Classify this cell by malaria status.
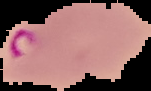

Parasitized.

From a thin blood film. Image is 151×91 pixels. Cell region segmented out of the field of view; the surrounding area is masked to black.